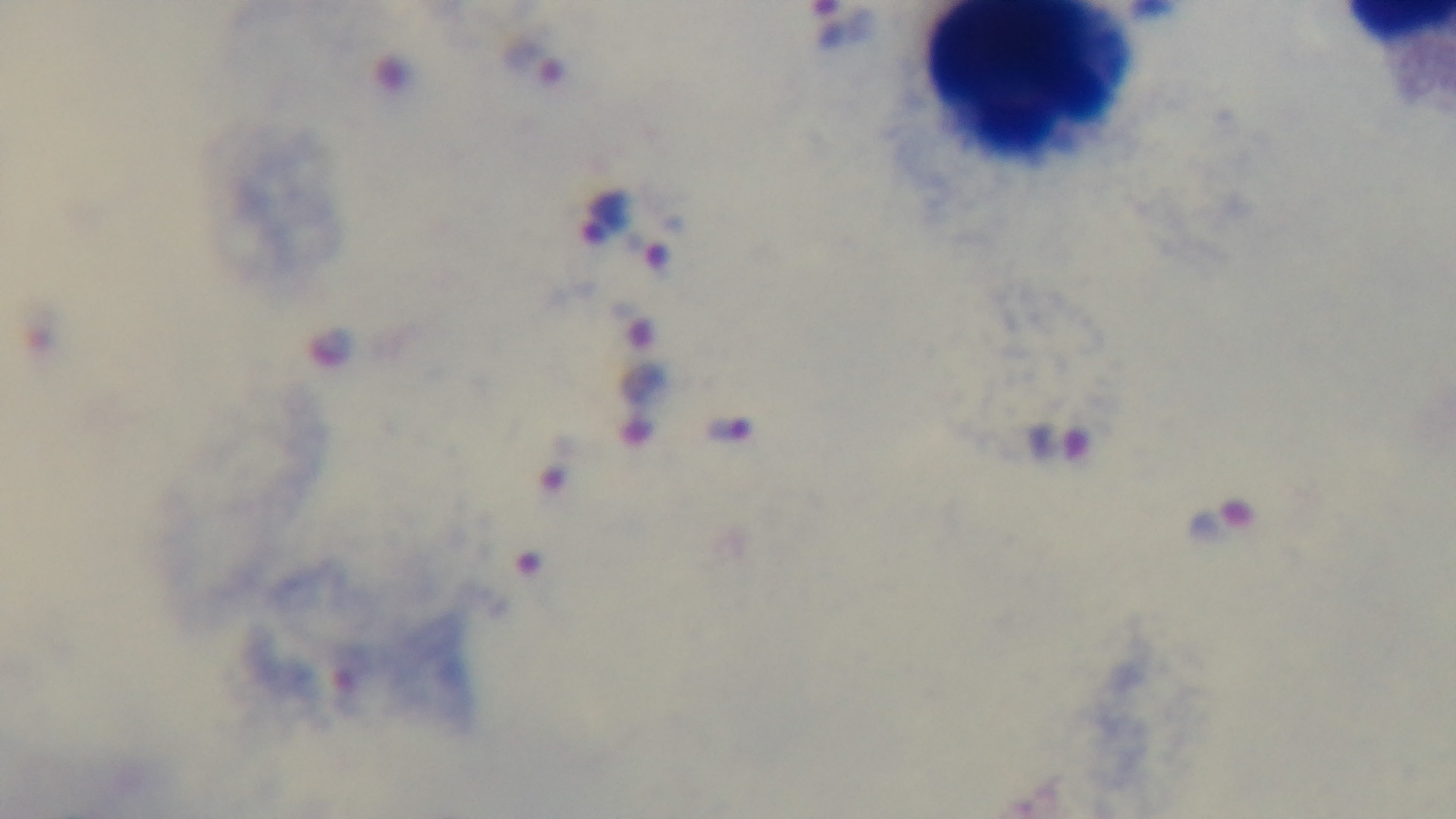

Photomicrograph. Single field of view. Malaria status: infected. Preparation: thick. Captured with a mounted 4K digital camera. Giemsa stain. Oil-immersion objective, 100x.